Point out each malaria parasite and each leukocyte.
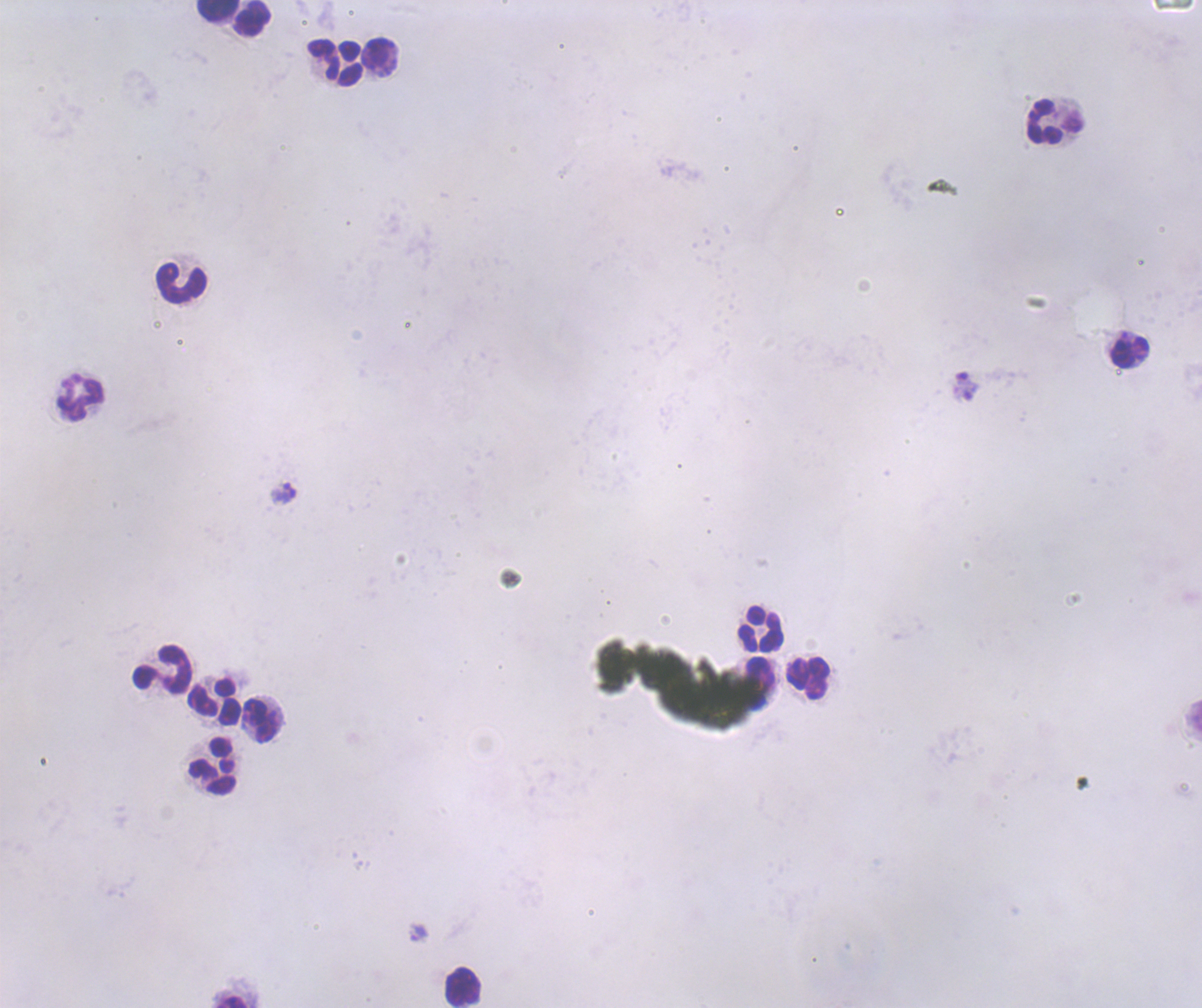

Approximate centers as {x, y} in pixels.
Trophozoites: {419, 932}.
No schizont or gametocyte forms observed.
Leukocytes: {218, 11}, {252, 18}, {323, 59}, {350, 63}, {1044, 122}, {181, 283}, {1130, 353}, {81, 399}, {760, 629}, {162, 669}, {808, 678}, {214, 702}, {260, 721}, {213, 766}, {462, 988}.

magnification = 100x
coloration quality = bad
image size = 1202×1008 pixels
background quality = poor
preparation = thick blood smear
context = previously used in an actual diagnosis
stain = Romanowsky
field of view = single